Find each parasitized RBC.
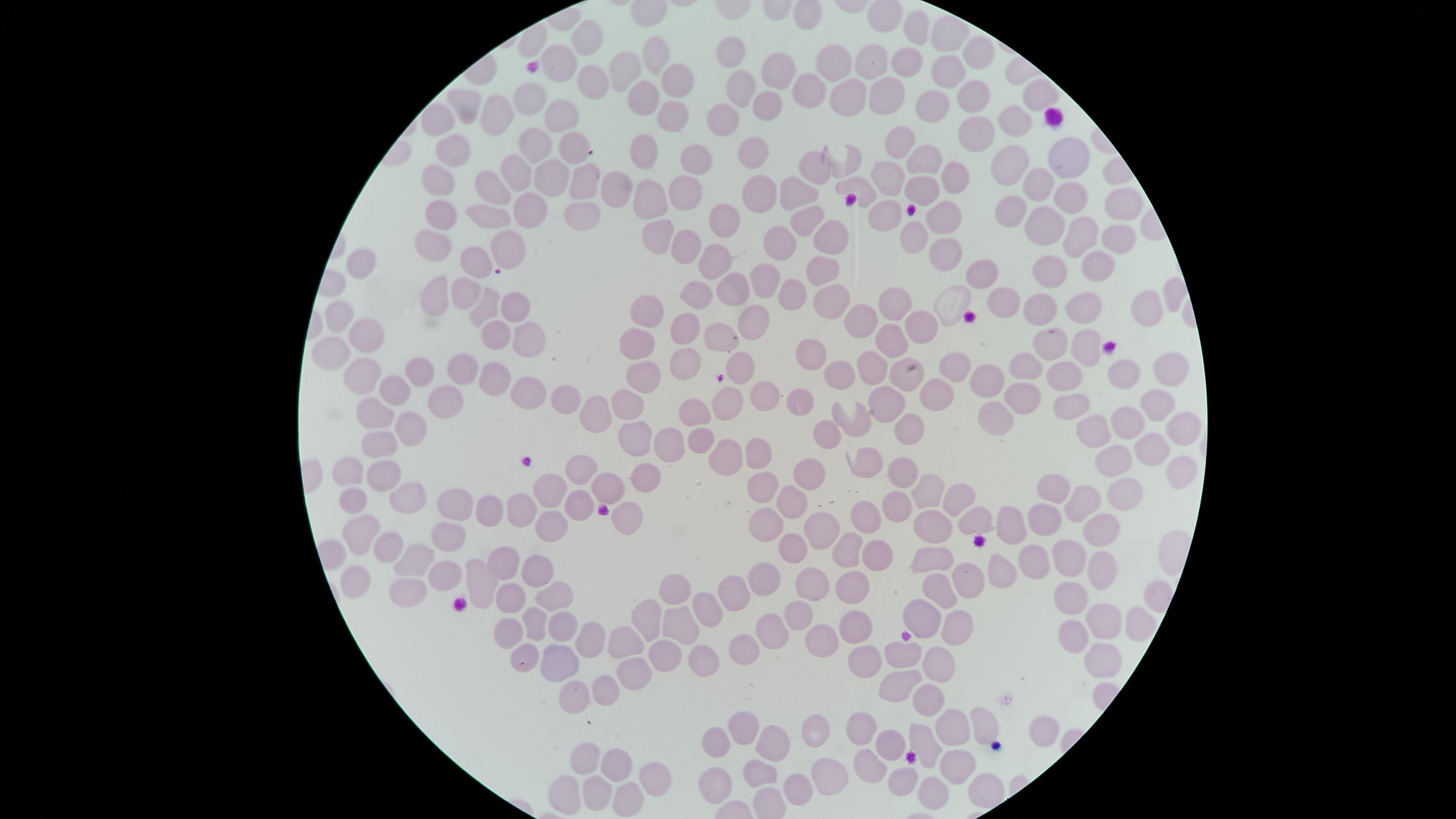

No parasitized RBCs identified.

capture: smartphone photograph through the microscope eyepiece
preparation: thin blood film
field_of_view: single
stain: Giemsa
image_size: 1456×819 pixels
uninfected_RBCs: 'approximate marker points as {x, y} in pixels: {915, 29}, {951, 34}, {589, 38}, {658, 51}, {979, 54}, {737, 55}, {561, 61}, {829, 61}, {870, 62}, {901, 65}, {625, 68}, {948, 69}, {779, 72}, {666, 79}, {592, 83}, {741, 89}, {810, 92}, {884, 92}, {978, 94}, {1038, 94}, {843, 99}, {530, 100}, {646, 103}, {468, 104}, {764, 104}, {936, 107}, {670, 110}, {563, 113}, {498, 115}, {1010, 117}, {439, 119}, {720, 119}, {973, 135}, {902, 141}, {534, 143}, {571, 147}, {456, 148}, {646, 150}, {750, 152}, {929, 158}, {1070, 159}, {693, 162}, {1013, 164}, {813, 165}, {508, 173}, {954, 173}, {886, 175}, {545, 177}, {439, 178}, {580, 181}, {624, 184}, {1036, 184}, {858, 185}, {491, 186}, {918, 186}, {754, 191}, {798, 191}, {684, 192}, {1060, 195}, {650, 203}, {529, 206}, {1011, 206}, {1119, 208}, {586, 210}, {875, 214}, {447, 216}, {493, 217}, {939, 217}, {720, 219}, {804, 219}, {1043, 227}, {914, 235}, {1083, 235}, {828, 238}, {500, 239}, {655, 239}, {771, 241}, {1113, 241}, {433, 242}, {683, 244}, {939, 251}, {713, 259}, {471, 265}, {1049, 268}, {822, 269}, {1091, 269}, {989, 272}, {362, 274}, {767, 278}, {726, 286}, {433, 293}, {789, 293}, {462, 294}, {691, 296}, {832, 296}, {891, 299}, {1003, 303}, {1081, 304}, {1140, 304}, {517, 305}, {480, 308}, {648, 309}, {1038, 309}, {340, 318}, {916, 320}, {757, 323}, {856, 323}, {683, 327}, {495, 332}, {366, 335}, {526, 335}, {717, 335}, {892, 337}, {1051, 340}, {1085, 344}, {814, 348}, {328, 351}, {640, 352}, {742, 361}, {957, 361}, {1028, 361}, {456, 365}, {684, 365}, {880, 365}, {1119, 371}, {1170, 373}, {842, 374}, {366, 375}, {418, 376}, {1066, 376}, {493, 378}, {906, 378}, {643, 379}, {987, 381}, {391, 389}, {933, 392}, {770, 394}, {524, 396}, {1023, 396}, {560, 397}, {725, 398}, {802, 398}, {886, 402}, {1154, 402}, {1076, 403}, {434, 405}, {595, 406}, {622, 406}, {701, 410}, {376, 412}, {1000, 413}, {1126, 422}, {407, 427}, {913, 429}, {1184, 430}, {1088, 431}, {830, 433}, {701, 437}, {637, 439}, {371, 443}, {676, 444}, {1155, 446}, {727, 448}, {754, 452}, {1119, 453}, {810, 468}, {580, 469}, {356, 471}, {901, 471}, {650, 474}, {1172, 479}, {386, 482}, {1056, 482}, {608, 485}, {766, 485}, {931, 492}, {545, 493}, {1120, 493}, {408, 496}, {1081, 496}, {795, 499}, {958, 500}, {358, 503}, {579, 504}, {456, 505}, {898, 505}, {489, 509}, {523, 510}, {625, 511}, {869, 514}, {1042, 518}, {971, 519}, {762, 524}, {818, 524}, {1019, 524}, {549, 525}, {929, 525}, {360, 535}, {1098, 535}, {386, 544}, {449, 544}, {795, 548}, {842, 549}, {879, 554}, {1069, 558}, {417, 562}, {928, 562}, {1046, 564}, {1098, 564}, {501, 565}, {530, 570}, {1000, 573}, {439, 574}, {362, 577}, {761, 577}, {972, 577}, {477, 580}, {852, 583}, {808, 586}, {669, 589}, {398, 590}, {939, 591}, {729, 593}, {558, 596}, {509, 597}, {1070, 599}, {706, 611}, {800, 611}, {916, 617}, {1106, 619}, {855, 620}, {953, 620}, {527, 623}, {637, 623}, {674, 625}, {562, 626}, {772, 628}, {502, 632}, {1068, 634}, {825, 638}, {588, 643}, {747, 645}, {623, 650}, {867, 654}, {899, 654}, {662, 655}, {523, 657}, {1103, 658}, {562, 664}, {934, 665}, {704, 666}, {630, 672}, {902, 677}, {604, 686}, {926, 698}, {571, 702}, {981, 721}, {955, 726}, {738, 729}, {1047, 730}, {812, 734}, {861, 735}, {765, 739}, {924, 740}, {890, 741}, {718, 743}, {960, 754}, {581, 760}, {612, 767}, {652, 768}, {868, 769}, {760, 771}, {827, 776}, {906, 777}, {796, 786}, {713, 789}, {934, 789}, {982, 789}, {589, 793}, {563, 795}, {629, 803}'
visible_region: circular